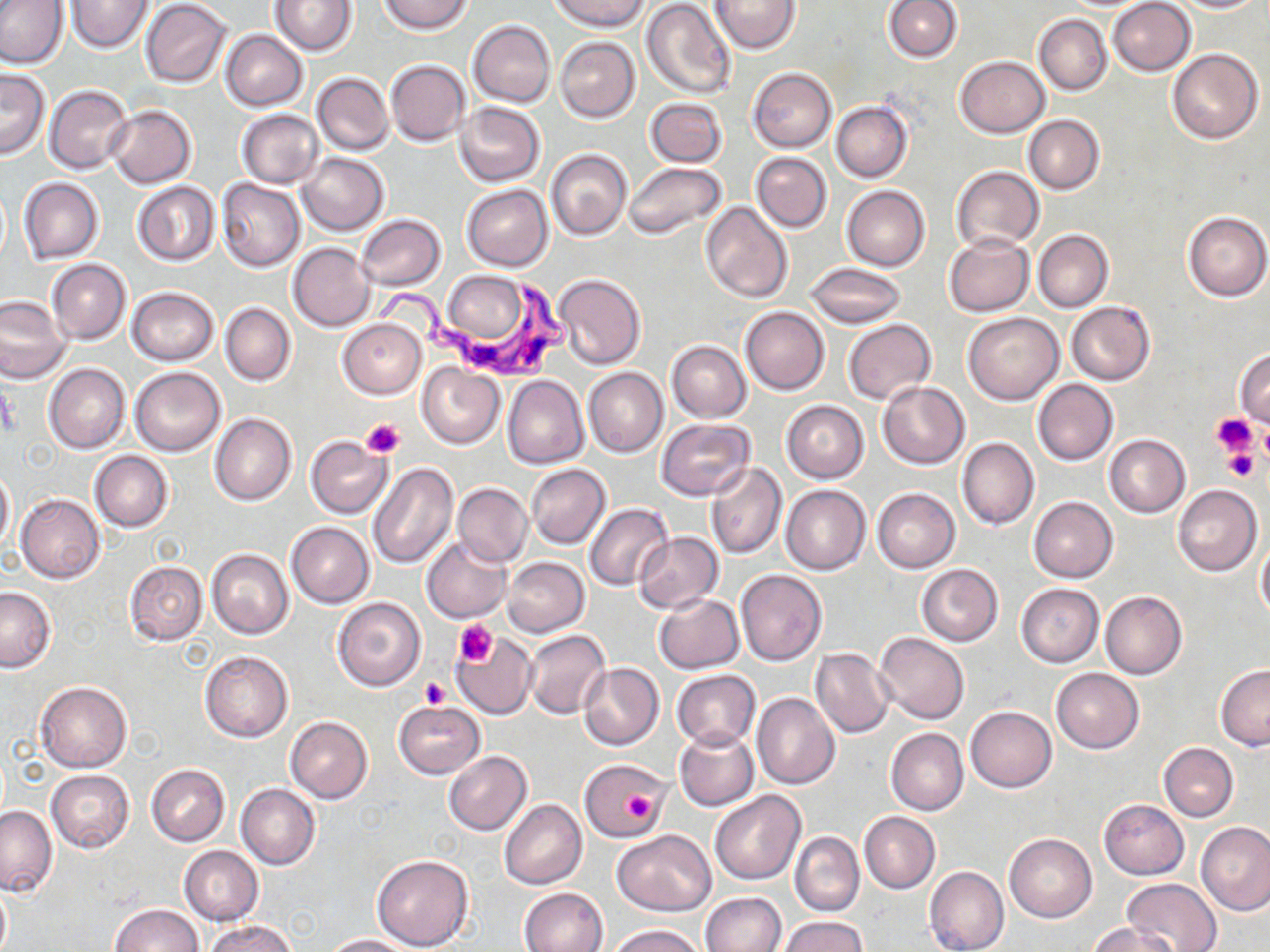 Approximate bounding boxes as (x1,y1)-(x2,y2) corner pairs in pixels. Platelet locations: (1212,412)-(1259,457), (360,419)-(405,459), (1258,420)-(1270,471), (1221,447)-(1260,481), (454,619)-(496,666), (419,678)-(448,709), (622,787)-(659,829). Uninfected red blood cell locations: (66,0)-(151,53), (271,0)-(354,55), (379,0)-(474,34), (552,0)-(647,30), (711,0)-(800,52), (1171,0)-(1263,12), (0,1)-(70,69), (139,1)-(232,87), (642,1)-(737,101), (884,1)-(961,61), (1108,1)-(1195,76), (1034,14)-(1112,95), (469,19)-(555,107), (220,30)-(307,110), (554,36)-(639,122), (1167,48)-(1262,145), (955,56)-(1049,136), (385,59)-(469,146), (747,67)-(836,152), (1,69)-(50,160), (313,73)-(393,155), (45,86)-(133,174), (646,97)-(726,167), (455,101)-(545,186), (832,101)-(913,182), (105,105)-(196,188), (236,109)-(324,188), (1024,115)-(1104,194), (546,149)-(631,239), (751,152)-(831,233), (297,153)-(390,236), (624,162)-(726,240), (951,165)-(1043,254), (19,178)-(101,263), (216,180)-(305,273), (132,181)-(219,264), (461,185)-(552,271), (843,185)-(929,271), (701,202)-(792,302), (1183,210)-(1270,301), (357,214)-(446,291), (1034,230)-(1113,312), (945,233)-(1034,317), (288,243)-(373,331), (47,259)-(131,344), (805,263)-(904,328), (553,272)-(647,370), (126,287)-(219,366), (0,296)-(73,383), (1066,302)-(1156,385), (220,304)-(295,386), (740,306)-(829,395), (963,312)-(1063,404), (339,319)-(425,398), (844,319)-(935,404), (670,321)-(828,407), (666,340)-(751,421), (1234,349)-(1270,430), (417,361)-(506,447), (43,363)-(129,454), (131,367)-(225,456), (584,367)-(668,457), (503,376)-(588,469), (1033,378)-(1118,466), (878,381)-(969,468), (782,400)-(868,483), (209,414)-(296,505), (655,419)-(754,501), (305,433)-(393,520), (1104,434)-(1190,517), (957,437)-(1038,530), (89,450)-(173,533), (368,462)-(458,568), (706,462)-(786,559), (527,464)-(609,548), (0,467)-(15,554), (453,482)-(531,566), (1173,484)-(1262,576), (781,485)-(871,574), (872,488)-(960,572), (16,494)-(105,582), (1028,496)-(1118,582), (584,501)-(674,592), (286,522)-(373,608), (633,531)-(722,613), (421,537)-(512,623), (1256,537)-(1270,621), (207,549)-(293,639), (501,557)-(589,637), (124,561)-(208,644), (916,564)-(1003,646), (736,569)-(827,666), (1017,583)-(1103,667), (0,586)-(55,672), (1100,591)-(1187,679), (655,593)-(743,674), (332,597)-(426,691), (522,628)-(611,720), (874,632)-(969,724), (451,634)-(540,719), (810,648)-(892,738), (200,651)-(293,743), (579,662)-(664,750), (1215,664)-(1270,750), (1051,668)-(1143,754), (672,670)-(760,750), (34,681)-(131,772), (753,693)-(840,790), (393,701)-(486,779), (966,706)-(1057,792), (284,716)-(373,803), (674,727)-(759,810), (885,728)-(968,815), (1159,743)-(1238,821), (443,751)-(532,835), (581,762)-(668,841), (146,764)-(228,846), (46,770)-(134,852), (236,784)-(320,870), (710,789)-(806,885), (1100,799)-(1188,879), (499,800)-(587,889), (0,805)-(57,896), (859,812)-(939,893), (1197,822)-(1270,916), (613,830)-(716,916), (790,832)-(863,915), (1005,833)-(1096,922), (179,846)-(263,925), (371,853)-(473,951), (925,865)-(1008,952), (1123,878)-(1220,951), (0,883)-(11,952), (518,887)-(608,952), (700,892)-(785,952), (109,903)-(202,952), (780,916)-(867,952), (205,919)-(297,952), (1086,922)-(1179,951), (608,924)-(708,952), (325,934)-(418,951). Trypanosoma brucei locations: (374,275)-(576,385). Slide-level diagnosis: Trypanosoma brucei. Captured at 1000x magnification. Thin blood film. Single field of view. Light microscopy. May-Grünwald-Giemsa stain. Image is 1270×952 pixels.